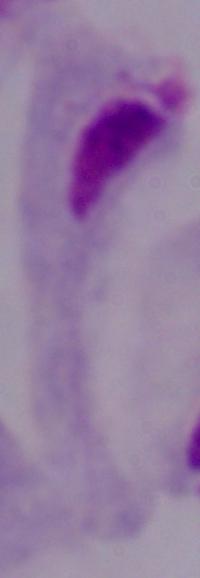 A trichomonad is shown. Captured at 1000x magnification. Photomicrograph.